Locate every blood parasite and identify its species.
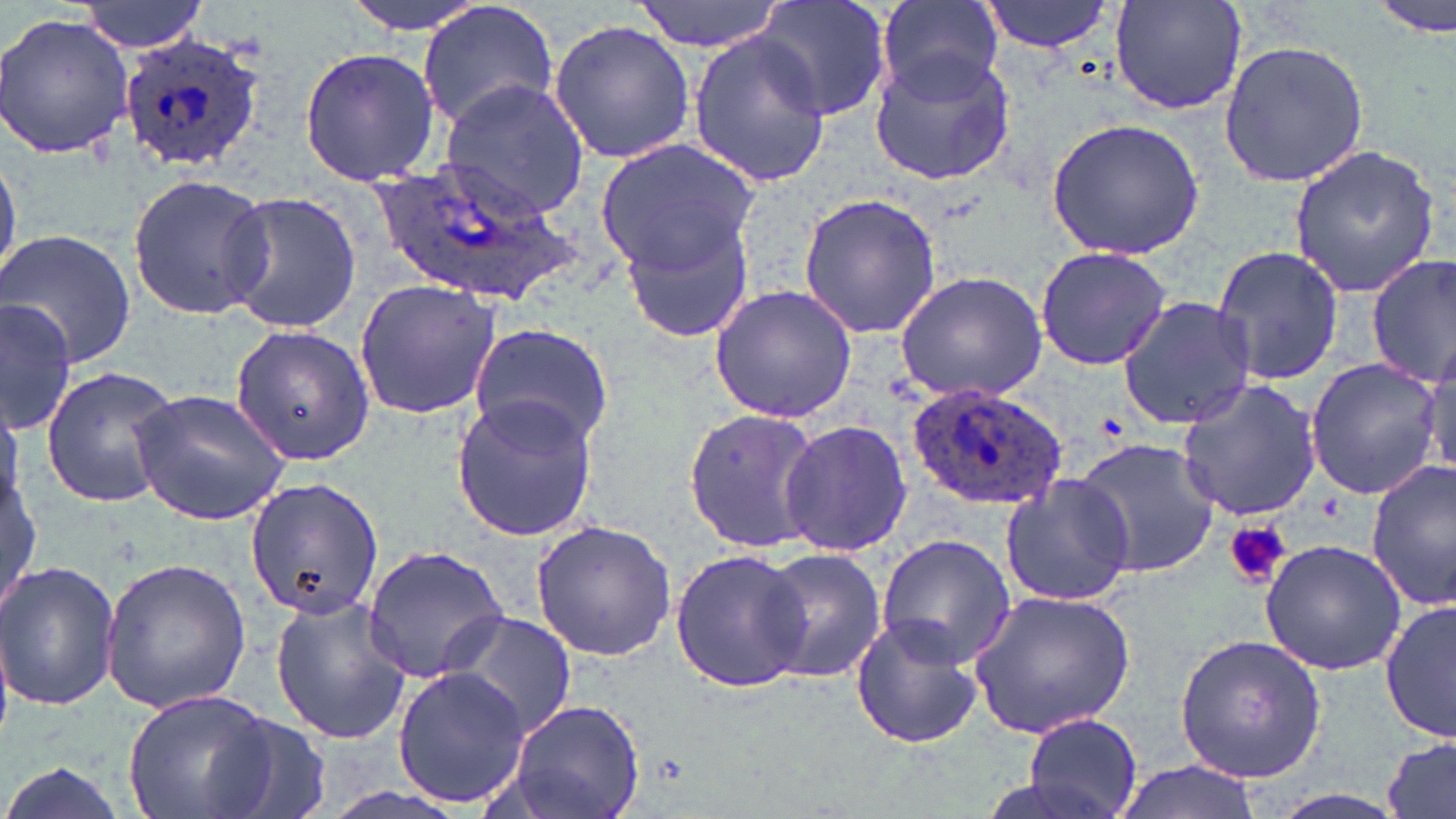
Approximate bounding boxes as [x1, y1, x2, y2] in pixels.
Plasmodium ovale-infected red blood cells: [118, 34, 269, 176], [367, 152, 585, 305], [906, 381, 1071, 512].
No Plasmodium falciparum, Plasmodium malariae, Plasmodium vivax, Babesia divergens, or Trypanosoma brucei observed.

slide-level diagnosis = Plasmodium ovale
modality = light microscopy
field of view = single
platelet locations = approximate bounding boxes as [x1, y1, x2, y2] in pixels: [1222, 522, 1293, 589]
stain = May-Grünwald-Giemsa
magnification = 1000x
uninfected red blood cell locations = approximate bounding boxes as [x1, y1, x2, y2] in pixels: [71, 0, 209, 53], [342, 0, 490, 35], [633, 0, 787, 51], [754, 0, 893, 122], [977, 0, 1115, 55], [1109, 0, 1247, 117], [1372, 0, 1454, 38], [875, 1, 1008, 98], [415, 2, 560, 135], [1, 10, 135, 161], [549, 18, 698, 166], [687, 31, 831, 189], [1217, 40, 1370, 187], [299, 47, 442, 185], [869, 49, 1017, 186], [439, 81, 591, 217], [1045, 118, 1206, 258], [594, 137, 762, 280], [1287, 143, 1443, 297], [0, 148, 21, 288], [126, 173, 275, 321], [216, 190, 365, 334], [798, 193, 941, 340], [607, 195, 764, 343], [0, 229, 137, 367], [1210, 244, 1346, 387], [1034, 246, 1173, 371], [1366, 252, 1455, 388], [894, 269, 1048, 402], [354, 278, 501, 420], [708, 284, 858, 423], [1116, 296, 1258, 430], [0, 298, 80, 433], [228, 323, 375, 467], [469, 324, 615, 452], [1422, 338, 1455, 485], [1304, 357, 1443, 501], [40, 364, 179, 509], [1175, 379, 1323, 521], [129, 388, 291, 526], [0, 390, 25, 511], [449, 394, 600, 542], [683, 407, 821, 554], [779, 419, 914, 557], [1072, 438, 1220, 579], [1366, 461, 1456, 609], [3, 464, 41, 617], [996, 472, 1138, 608], [245, 475, 384, 619], [530, 519, 678, 661], [875, 534, 1016, 670], [1258, 539, 1407, 676], [363, 545, 510, 684], [757, 547, 887, 686], [669, 548, 812, 693], [101, 555, 250, 715], [0, 562, 123, 713], [965, 588, 1135, 738], [268, 593, 412, 743], [1381, 598, 1456, 745], [436, 609, 578, 741], [850, 616, 986, 751], [1173, 633, 1328, 782], [393, 665, 528, 810], [121, 688, 284, 819], [506, 696, 645, 819], [1022, 711, 1143, 818], [199, 712, 331, 819], [1382, 735, 1456, 819], [1114, 759, 1262, 819], [0, 760, 130, 819]
image size = 1456×819 pixels
preparation = thin blood smear